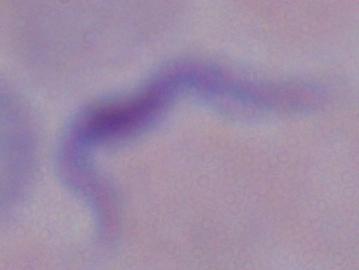

A trypanosome is seen. Micrograph. 1000x magnification.